Report the malaria status of this cell.
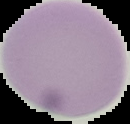
Uninfected.

preparation = thin blood film
image size = 130×124 pixels
image type = segmented cell region on a black background